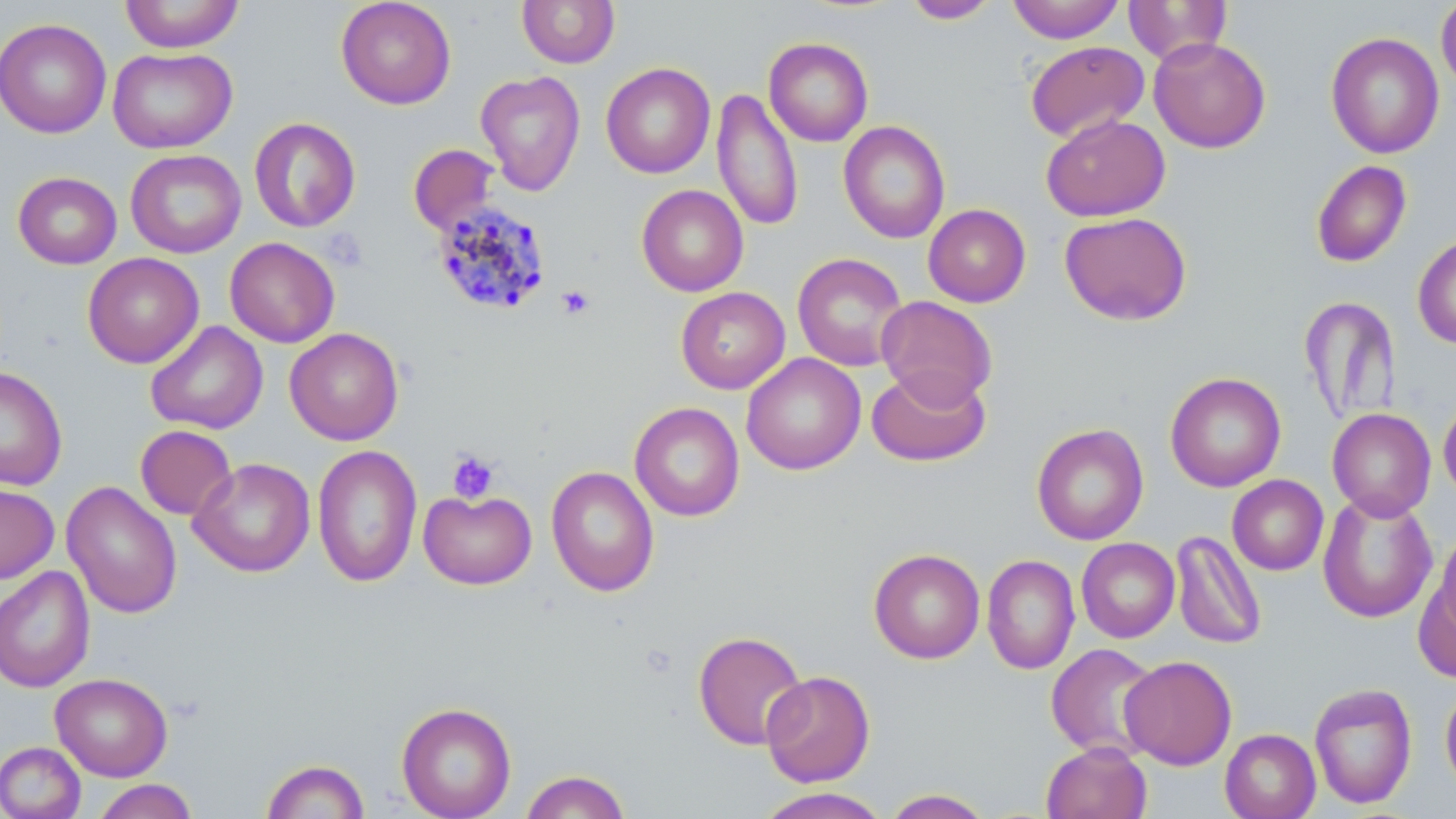
Summary:
  - Coordinate format: approximate bounding boxes as (x1, y1, x2, y2) in pixels
  - Platelet locations: (323, 228, 366, 270), (555, 284, 595, 320), (447, 450, 500, 504)
  - Uninfected red blood cell locations: (119, 0, 244, 52), (335, 0, 457, 109), (517, 0, 620, 68), (903, 0, 1001, 24), (1007, 0, 1126, 43), (1123, 0, 1233, 66), (1436, 0, 1456, 93), (0, 18, 112, 139), (1325, 31, 1445, 159), (1148, 36, 1271, 154), (763, 37, 874, 147), (1025, 40, 1150, 143), (107, 46, 238, 153), (601, 62, 716, 179), (475, 70, 586, 197), (711, 88, 804, 231), (1041, 114, 1170, 222), (249, 117, 361, 233), (838, 120, 950, 244), (408, 144, 500, 235), (125, 149, 246, 258), (1311, 160, 1412, 267), (12, 171, 122, 269), (636, 184, 748, 297), (923, 204, 1031, 307), (1059, 211, 1192, 326), (1412, 234, 1456, 349), (225, 237, 340, 348), (82, 252, 204, 369), (792, 252, 909, 371), (676, 287, 790, 394), (876, 295, 997, 407), (1299, 296, 1401, 426), (145, 320, 268, 435), (285, 327, 404, 445), (741, 353, 866, 475), (867, 364, 991, 467), (0, 366, 68, 491), (1165, 371, 1286, 492), (1438, 396, 1456, 503), (629, 402, 745, 522), (1327, 408, 1436, 520), (1031, 423, 1149, 546), (135, 425, 237, 520), (313, 444, 422, 588), (188, 458, 316, 577), (545, 465, 660, 597), (1227, 474, 1329, 576), (61, 480, 182, 619), (0, 482, 59, 585), (419, 489, 537, 590), (1317, 492, 1438, 623), (1434, 526, 1456, 640), (1170, 530, 1267, 650), (1077, 537, 1180, 643), (868, 548, 985, 664), (982, 554, 1080, 674), (0, 566, 95, 692), (1415, 569, 1456, 683), (693, 630, 808, 751), (1045, 643, 1162, 761), (1120, 655, 1237, 769), (760, 670, 875, 787), (50, 672, 173, 781), (1308, 682, 1418, 809), (1440, 682, 1456, 797), (397, 702, 516, 819), (1220, 728, 1320, 819), (0, 741, 86, 819), (1041, 742, 1151, 819), (261, 759, 370, 819), (519, 769, 632, 818), (92, 779, 198, 819), (752, 787, 893, 819), (881, 789, 995, 818)
  - Plasmodium malariae-infected red blood cell locations: (431, 200, 551, 316)
  - Slide-level diagnosis: Plasmodium malariae
  - Image size: 1456×819 pixels
  - Preparation: thin blood film
  - Stain: May-Grünwald-Giemsa
  - Field of view: one of a larger specimen
  - Magnification: 1000x
  - Modality: light microscopy